State which parasite is depicted.
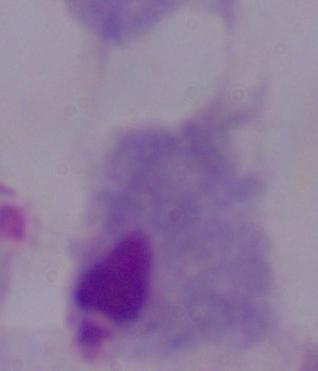
This is a trichomonad.

magnification = 1000x
modality = micrograph